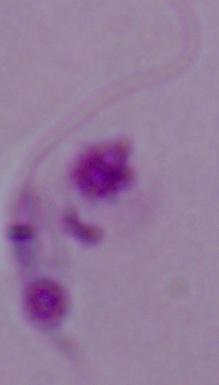
modality: photomicrograph
identification: Leishmania
magnification: 1000x